Classify this cell by malaria status.
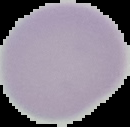

It is uninfected.

Summary:
  - Preparation: thin blood film
  - Image size: 130×127 pixels
  - Image type: cell region segmented out of the field of view; surrounding area masked to black